Locate every uninfected red blood cell.
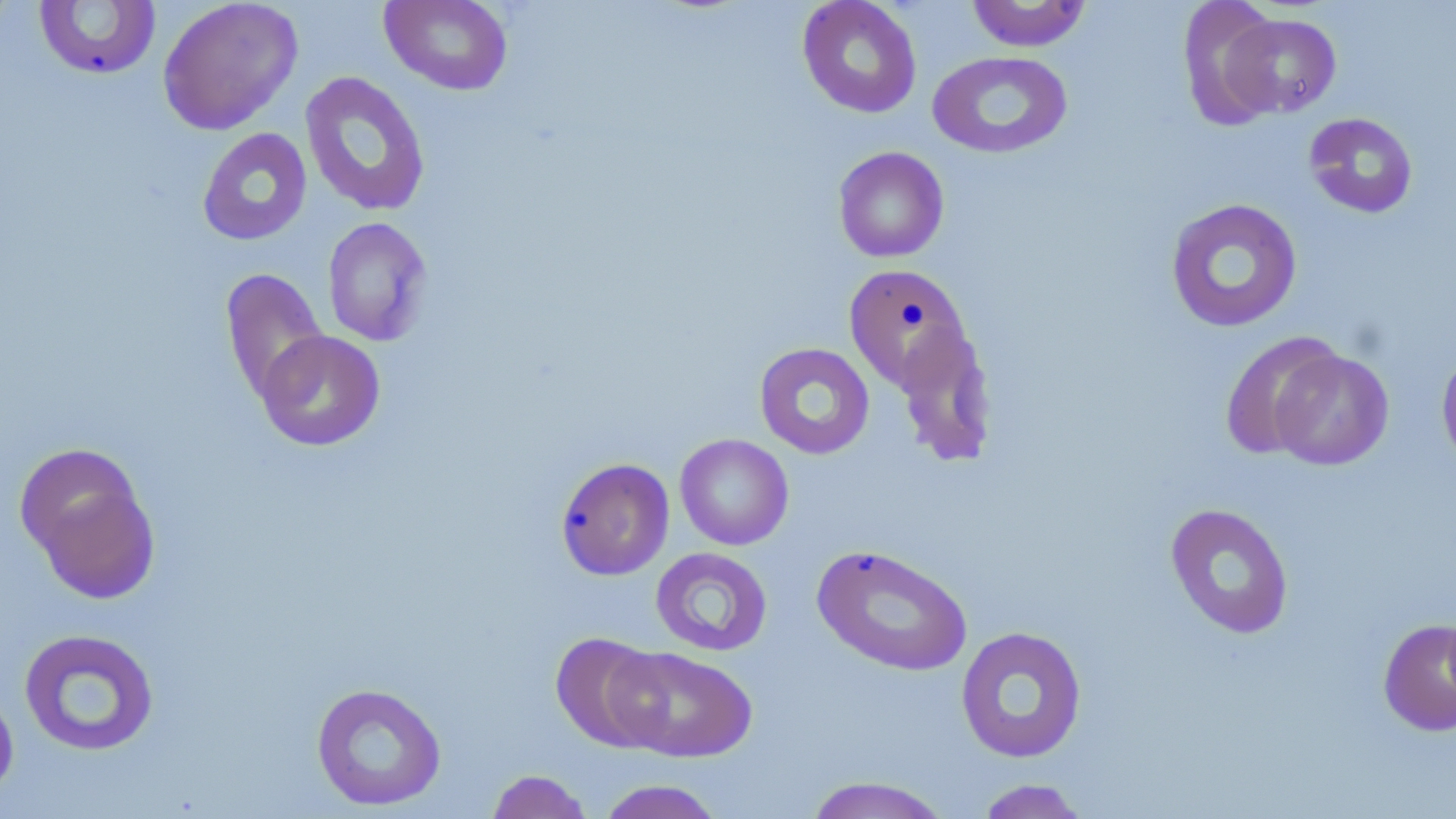

Approximate bounding boxes as (x1,y1)-(x2,y2) corner pairs in pixels.
Uninfected red blood cells: (157,0)-(304,135), (380,0)-(514,96), (797,0)-(923,118), (965,0)-(1092,52), (1177,0)-(1284,129), (32,1)-(162,81), (1220,12)-(1342,119), (927,50)-(1073,159), (299,70)-(431,216), (1303,112)-(1419,219), (197,127)-(312,246), (832,146)-(949,263), (1165,198)-(1303,333), (321,216)-(434,346), (843,264)-(975,395), (220,268)-(328,403), (891,324)-(998,466), (255,330)-(386,452), (1219,331)-(1344,460), (754,342)-(874,459), (1269,348)-(1395,471), (1436,348)-(1456,474), (674,433)-(794,551), (16,443)-(161,601), (556,457)-(675,581), (1165,503)-(1295,640), (812,543)-(974,677), (650,547)-(773,656), (1377,618)-(1456,737), (955,625)-(1088,764), (18,627)-(160,757), (550,632)-(671,752), (608,645)-(758,763), (310,682)-(447,811), (0,685)-(19,802), (485,769)-(595,819), (801,776)-(953,818), (974,778)-(1093,818), (596,779)-(726,819).

Summary:
  - Slide-level diagnosis: no evidence of blood parasites
  - Stain: May-Grünwald-Giemsa
  - Modality: optical microscopy
  - Field of view: single
  - Magnification: 1000x
  - Image size: 1456×819 pixels
  - Preparation: thin blood film